Identify the blood parasite species.
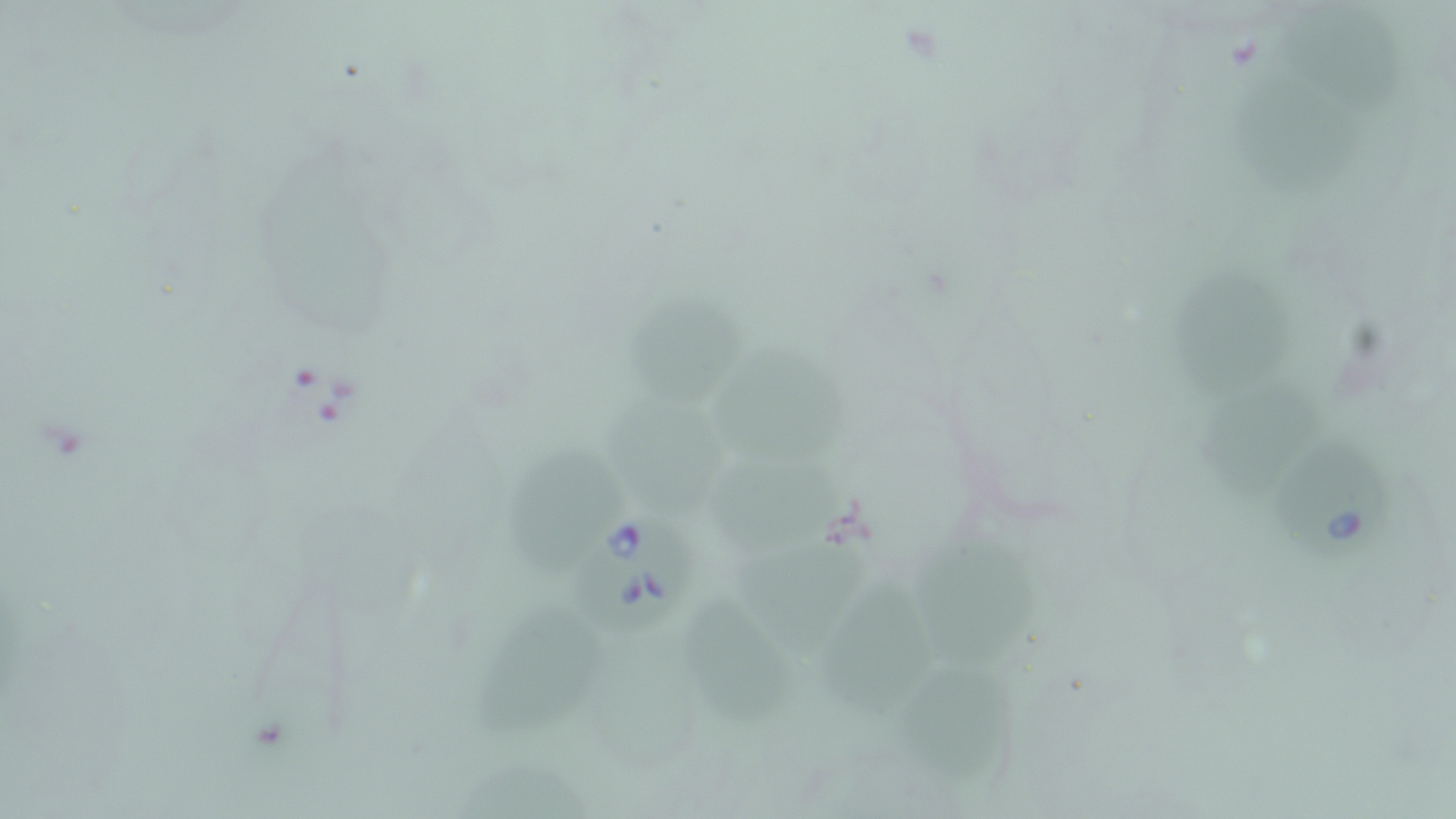
Babesia divergens.

{
  "field_of_view": "one of a larger specimen",
  "preparation": "thin blood smear",
  "babesia_divergens_infected_red_blood_cell_locations": "approximate bounding boxes as [x1, y1, x2, y2] in pixels: [1271, 445, 1397, 560], [562, 508, 701, 635]",
  "modality": "light microscopy",
  "stain": "May-Grünwald-Giemsa",
  "magnification": "1000x",
  "uninfected_red_blood_cell_locations": "approximate bounding boxes as [x1, y1, x2, y2] in pixels: [1274, 1, 1409, 119], [1239, 79, 1366, 201], [1166, 275, 1292, 401], [618, 292, 748, 412], [712, 351, 850, 461], [1203, 379, 1322, 496], [609, 394, 732, 517], [503, 444, 633, 575], [701, 449, 850, 556], [723, 533, 871, 661], [916, 544, 1039, 669], [818, 572, 942, 721], [685, 600, 794, 732], [476, 614, 609, 740], [904, 667, 1016, 780], [457, 757, 602, 819]",
  "image_size": "1456×819 pixels"
}